Describe the morphology of the erythrocytes.
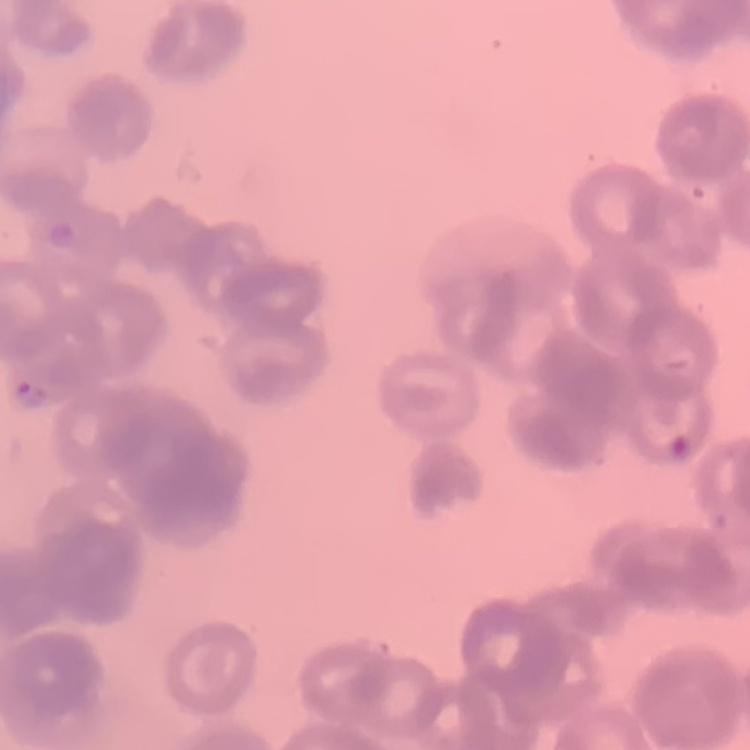

Rouleaux formation.

Stained with either Field's or Giemsa. One tile cut from a larger photomicrograph. Thin blood smear.